Identify the cell.
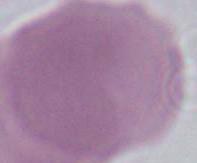

An erythrocyte.

modality = photomicrograph
magnification = 1000x